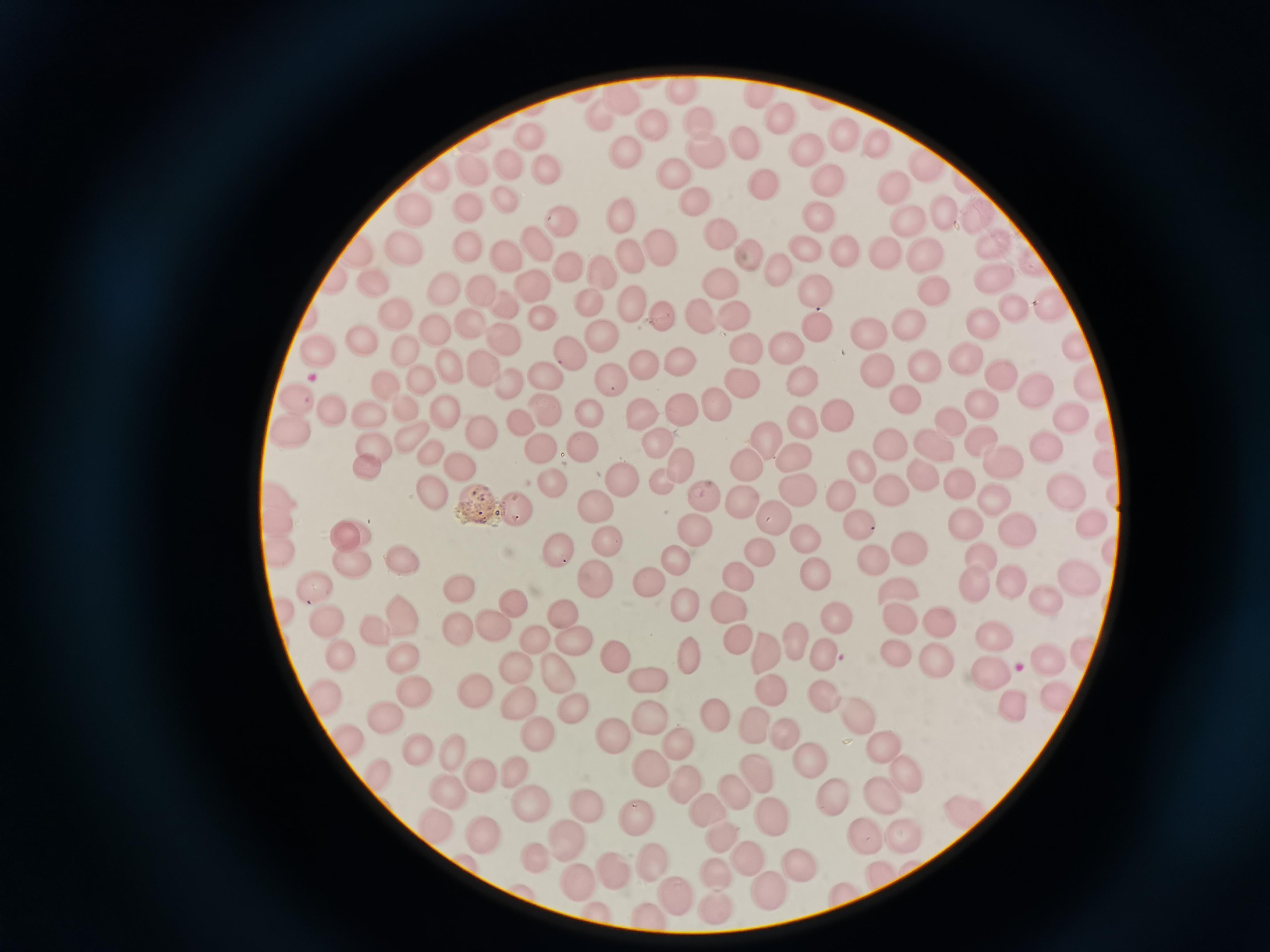

Approximate centers as [x, y] in pixels. Cell locations: [680, 88], [758, 94], [622, 100], [698, 115], [778, 116], [603, 120], [653, 124], [845, 133], [530, 136], [744, 141], [877, 144], [806, 148], [705, 149], [627, 156], [924, 164], [510, 165], [547, 165], [474, 170], [434, 176], [827, 176], [679, 178], [766, 181], [893, 187], [504, 197], [696, 205], [408, 208], [472, 208], [941, 211], [974, 214], [619, 216], [559, 219], [823, 220], [905, 221], [718, 237], [994, 240], [468, 241], [537, 241], [658, 246], [804, 247], [360, 248], [402, 250], [882, 250], [846, 253], [925, 254], [498, 256], [751, 256], [627, 258], [569, 266], [782, 268], [602, 271], [994, 274], [338, 275], [374, 280], [533, 282], [442, 286], [719, 286], [935, 287], [818, 290], [481, 291], [506, 301], [586, 301], [634, 303], [1008, 304], [1049, 307], [543, 313], [701, 313], [309, 316], [397, 318], [738, 318], [661, 319], [908, 320], [987, 321], [475, 322], [815, 325], [436, 330], [869, 332], [505, 339], [599, 339], [361, 340], [741, 345], [1079, 345], [319, 349], [407, 351], [788, 352], [964, 356], [571, 361], [677, 362], [642, 364], [440, 365], [878, 366], [925, 367], [483, 369], [1087, 375], [1001, 378], [544, 381], [741, 381], [420, 382], [611, 382], [803, 382], [510, 384], [1034, 384], [384, 386], [295, 398], [900, 398], [714, 402], [980, 403], [681, 407], [406, 408], [327, 411], [441, 411], [589, 411], [640, 412], [542, 413], [1074, 415], [371, 416], [838, 416], [948, 417], [803, 425], [288, 428], [521, 428], [478, 429], [768, 437], [981, 438], [413, 439], [888, 439], [932, 439], [658, 440], [376, 445], [1046, 447], [586, 449], [539, 454], [790, 454], [429, 455], [863, 460], [678, 462], [363, 463], [1000, 463], [746, 464], [462, 465], [1107, 467], [920, 470], [659, 476], [550, 480], [624, 484], [797, 485], [892, 485], [965, 485], [1060, 490], [428, 493], [842, 496], [992, 496], [275, 498], [738, 499], [706, 500], [513, 509], [595, 509], [773, 515], [1089, 518], [857, 521], [271, 523], [1011, 524], [964, 525], [693, 533], [352, 534], [609, 538], [813, 541], [911, 546], [278, 553], [558, 553], [759, 556], [985, 557], [674, 558], [351, 560], [405, 560], [871, 562], [1079, 574], [740, 576], [818, 578], [594, 579], [1013, 580], [653, 582], [973, 583], [316, 587], [897, 593], [459, 595], [1049, 599], [512, 604], [725, 604], [685, 608], [564, 612], [279, 614], [398, 614], [940, 618], [838, 620], [898, 621], [325, 622], [455, 624], [490, 624], [380, 635], [996, 636], [537, 640], [574, 640], [739, 640], [798, 645], [772, 649], [613, 652], [1082, 652], [902, 654], [1042, 656], [935, 657], [691, 658], [825, 659], [342, 660], [405, 661], [991, 666], [515, 670], [557, 673], [642, 675], [770, 684], [477, 694], [319, 697], [409, 698], [1001, 698], [822, 699], [1058, 700], [521, 703], [574, 707], [653, 715], [856, 715], [720, 717], [383, 719], [756, 722], [535, 733], [785, 733], [880, 737], [613, 740], [353, 744], [672, 745], [418, 748], [453, 754], [651, 765], [814, 767], [517, 771], [908, 771], [486, 775], [381, 778], [760, 778], [684, 782], [451, 788], [886, 791], [735, 793], [836, 795], [533, 800], [588, 805], [705, 805], [633, 818], [771, 818], [439, 827], [721, 830], [903, 832], [484, 834], [871, 835], [570, 839], [538, 855], [648, 859], [748, 860], [801, 864], [613, 867], [715, 869], [879, 871], [581, 880], [765, 885], [676, 889], [842, 889]. Giemsa-stained preparation. Image is 1270×952 pixels. One field from this slide. Thin blood film. Acquired by smartphone through the microscope eyepiece.